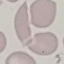 Malaria status: uninfected. Giemsa stain. Acquired by smartphone through the microscope eyepiece. Thin blood smear. Cell patch, automatically extracted from a larger field of view and resized to 64 × 64 pixels.